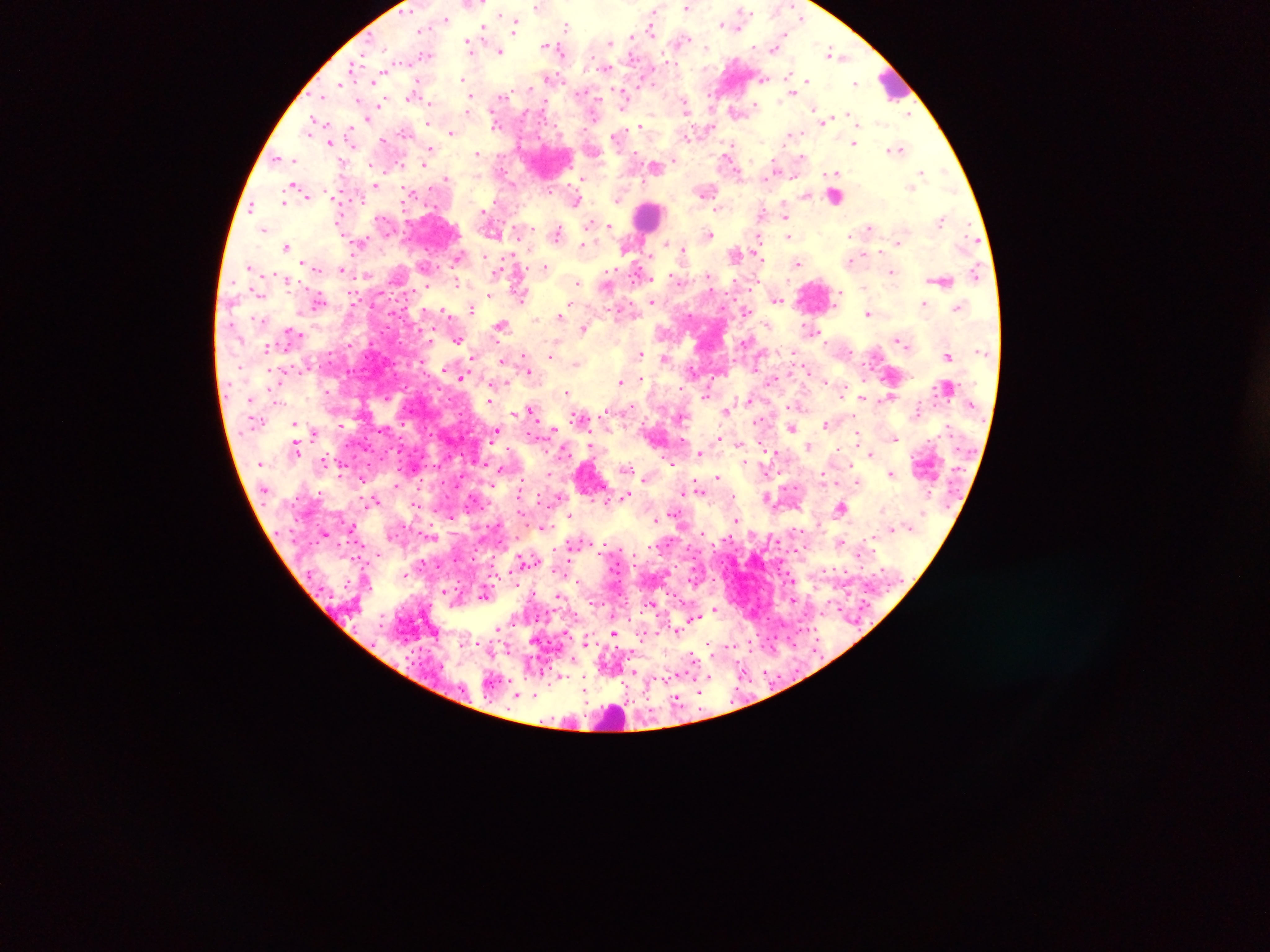
Approximate centers as x y in pixels.
Summary:
  - Malaria parasite locations: 540 7; 688 7; 742 12; 654 13; 446 18; 802 18; 515 24; 726 24; 567 26; 651 26; 483 27; 632 36; 683 39; 609 43; 470 45; 553 46; 776 47; 500 51; 426 55; 838 55; 353 67; 606 67; 548 78; 465 79; 806 81; 856 83; 415 91; 791 92; 624 95; 323 97; 471 98; 382 101; 429 103; 684 105; 756 106; 815 109; 736 111; 909 112; 369 115; 848 116; 825 119; 495 120; 314 125; 640 125; 451 132; 793 133; 618 135; 686 136; 384 139; 331 142; 855 142; 430 148; 896 149; 477 153; 802 156; 279 158; 402 164; 656 166; 775 166; 922 172; 448 178; 582 178; 376 185; 912 186; 296 187; 706 189; 411 193; 806 195; 577 199; 618 199; 284 202; 252 206; 720 208; 785 214; 942 219; 609 225; 870 226; 263 229; 558 232; 709 235; 758 236; 789 236; 360 241; 900 242; 667 244; 585 245; 287 246; 627 246; 683 250; 736 253; 459 256; 852 259; 304 262; 798 262; 249 265; 545 265; 342 269; 499 270; 641 271; 892 272; 976 273; 942 280; 576 281; 458 282; 608 284; 521 295; 488 296; 776 298; 651 301; 925 303; 472 307; 959 307; 444 310; 869 312; 561 315; 537 318; 502 325; 584 328; 810 329; 292 330; 458 340; 899 340; 747 342; 267 346; 551 354; 639 354; 948 356; 665 358; 472 359; 504 360; 526 364; 577 364; 528 370; 692 370; 463 375; 640 377; 622 383; 329 392; 568 392; 707 394; 890 395; 862 397; 749 399; 490 400; 796 405; 631 407; 532 409; 726 410; 917 413; 580 417; 760 422; 826 423; 295 424; 340 425; 792 428; 553 429; 315 431; 496 431; 859 434; 894 437; 718 438; 810 445; 297 446; 591 447; 839 447; 700 453; 870 454; 323 460; 671 462; 745 462; 502 468; 892 472; 822 474; 362 478; 718 478; 646 479; 858 481; 697 485; 629 494; 767 496; 375 501; 417 504; 842 508; 521 510; 675 512; 570 515; 736 518; 655 519; 352 528; 325 533; 841 543; 861 554; 525 561; 405 574; 577 582; 560 595; 653 603; 715 609; 695 617; 498 628; 677 630; 615 632; 587 642; 750 648; 694 659; 559 676; 709 676; 656 677; 585 682; 519 693
  - Leukocyte locations: 894 84; 839 194; 648 216; 814 295; 615 717
  - Image size: 1270×952 pixels
  - Country: Ghana
  - Field of view: single
  - Capture: mobile-phone photograph through a microscope
  - Preparation: thick blood film